Identify the parasite.
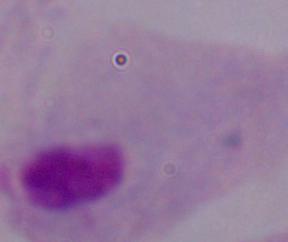
This is a trichomonad.

Summary:
  - Magnification: 1000x
  - Modality: photomicrograph